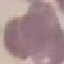

Malaria status: uninfected. Giemsa stain. Automatically extracted cell patch, resized to 64 × 64 pixels. Acquired by smartphone through the microscope eyepiece. Thin blood smear.